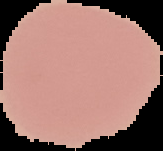

Malaria status: uninfected. Segmented cell region on a black background. Image is 163×151 pixels. From a thin blood film.